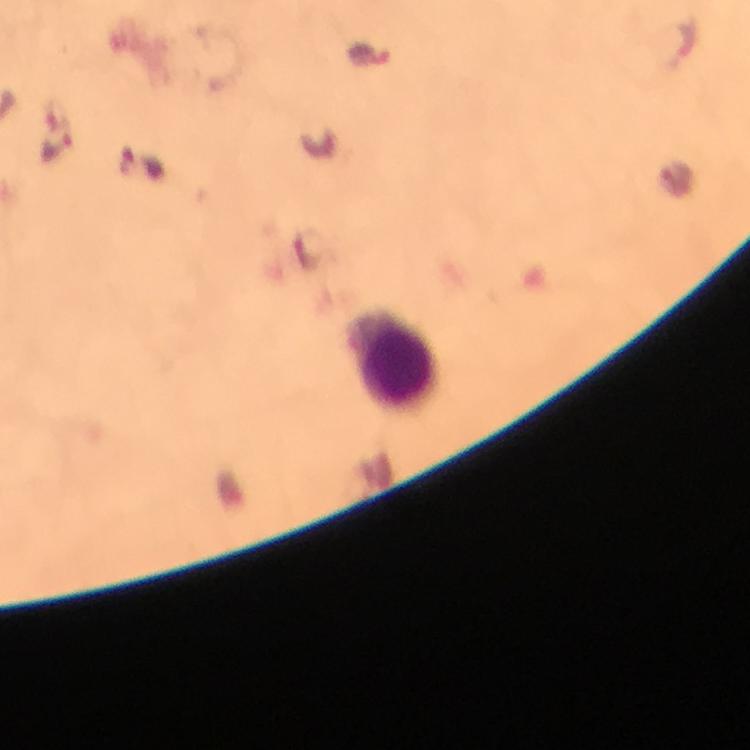
Approximate object centers, in pixels from the top-left corner.
Summary:
  - Leukocyte locations: (x=393, y=360)
  - Plasmodium parasite locations: (x=680, y=41), (x=368, y=53), (x=58, y=149)
  - Image size: 750×750 pixels
  - Capture: smartphone photograph through a microscope
  - Magnification: 100x
  - Stain: Giemsa
  - Context: from a diagnostic examination for malaria
  - Cropped from: one field of view
  - Preparation: thick blood film
  - Immersion oil: applied